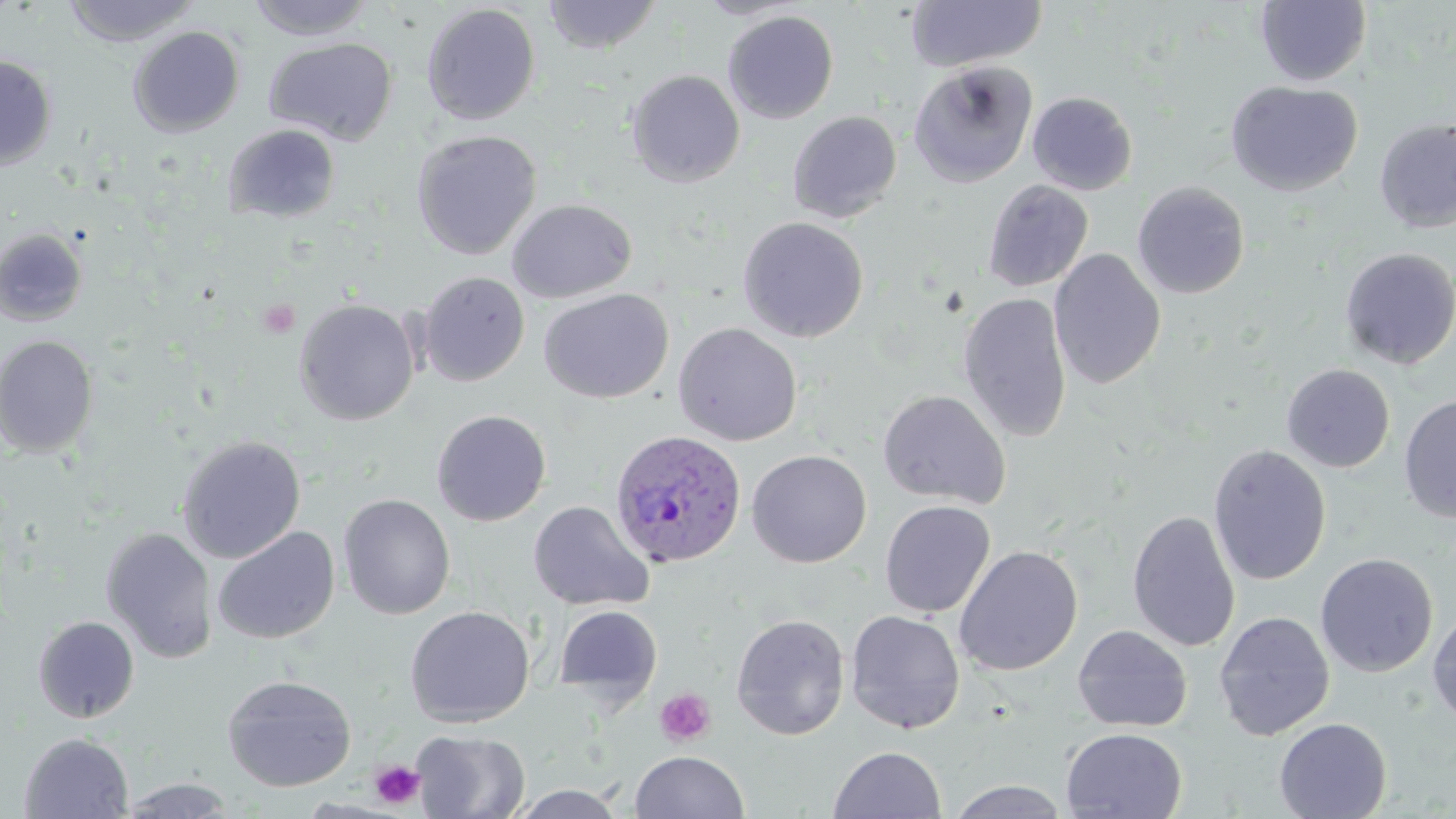

Approximate bounding boxes as (x1, y1, x2, y2) in pixels. Plasmodium ovale-infected red blood cell locations: (609, 429, 747, 569). Uninfected red blood cell locations: (61, 0, 201, 47), (245, 0, 378, 41), (541, 0, 662, 55), (696, 0, 805, 19), (905, 1, 1047, 73), (1255, 1, 1371, 86), (420, 3, 541, 126), (723, 10, 839, 124), (128, 26, 244, 138), (264, 37, 398, 145), (0, 54, 57, 171), (908, 60, 1038, 188), (626, 70, 745, 187), (1225, 80, 1363, 197), (1027, 92, 1137, 195), (787, 111, 902, 223), (1374, 119, 1456, 233), (222, 124, 341, 224), (411, 130, 541, 260), (982, 180, 1094, 292), (1132, 181, 1250, 299), (506, 199, 637, 303), (737, 216, 869, 342), (0, 227, 88, 326), (1339, 246, 1455, 369), (1048, 249, 1166, 391), (418, 271, 529, 386), (538, 289, 674, 404), (958, 292, 1072, 442), (294, 298, 420, 426), (673, 322, 803, 446), (0, 335, 99, 458), (1282, 364, 1395, 472), (876, 389, 1012, 508), (1398, 395, 1456, 525), (431, 409, 552, 526), (176, 435, 306, 563), (1208, 444, 1331, 585), (746, 449, 872, 568), (338, 494, 455, 620), (528, 500, 653, 611), (879, 500, 996, 618), (1127, 509, 1240, 652), (213, 526, 340, 645), (100, 528, 218, 664), (953, 545, 1083, 676), (1315, 553, 1438, 677), (554, 604, 663, 705), (404, 606, 535, 727), (1427, 608, 1456, 730), (845, 609, 965, 734), (1214, 611, 1335, 741), (730, 613, 850, 741), (33, 616, 139, 723), (1072, 624, 1193, 732), (221, 675, 357, 792), (1274, 717, 1392, 819), (1061, 727, 1188, 818), (411, 729, 530, 819), (19, 733, 134, 818), (828, 746, 947, 818), (630, 750, 749, 819), (116, 777, 240, 818), (945, 779, 1073, 819), (508, 785, 628, 819). Platelet locations: (257, 298, 300, 339), (654, 688, 716, 747), (369, 760, 425, 809). Slide-level diagnosis: Plasmodium ovale. Thin blood film. May-Grünwald-Giemsa stain. Light microscopy. Image is 1456×819 pixels. Captured at 1000x magnification. Single field of view.